Evaluate for malaria.
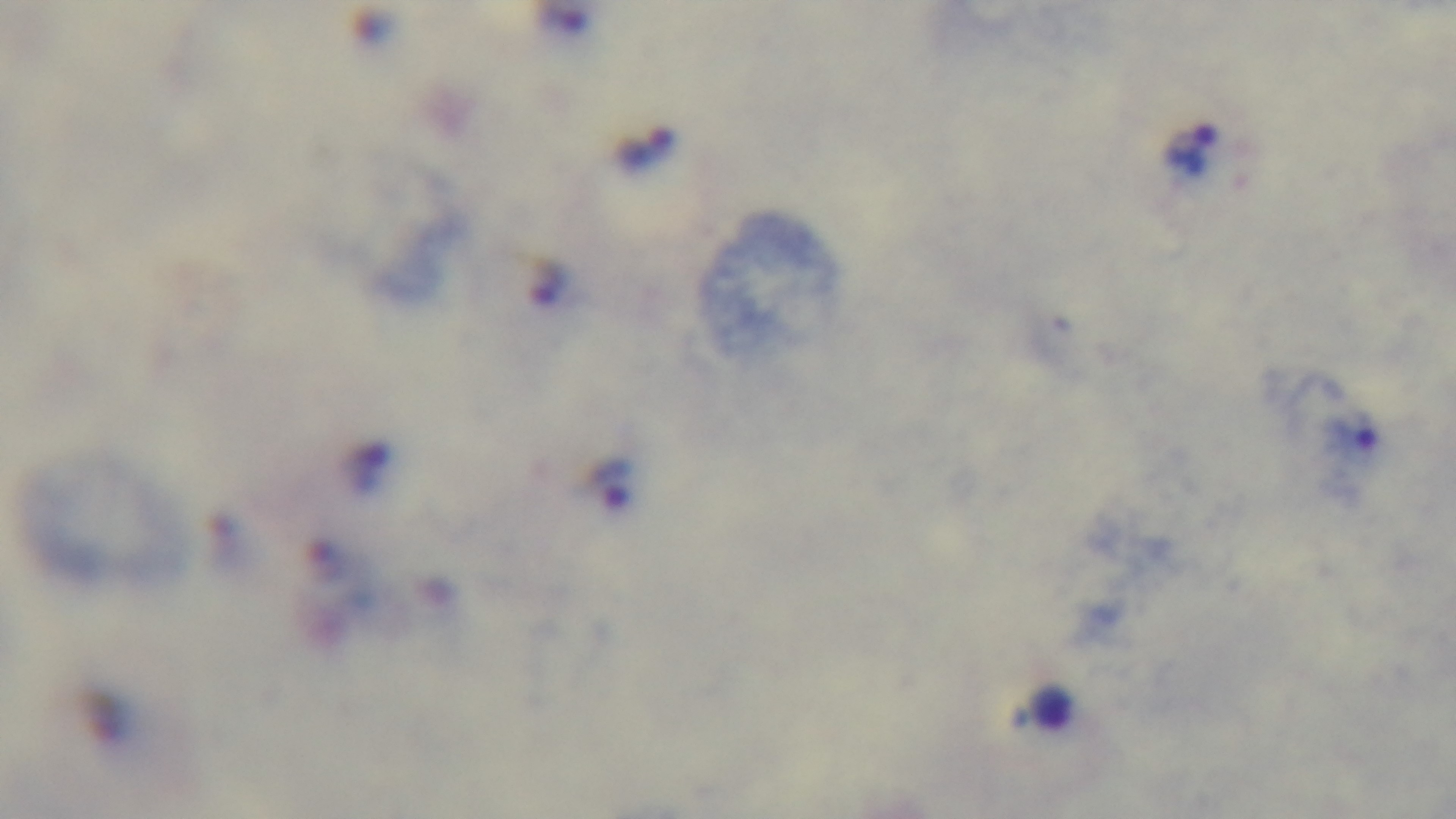

It is infected.

objective = 100x oil immersion
field of view = single
stain = Giemsa
modality = light microscopy
preparation = thick
capture = mounted 4K digital camera